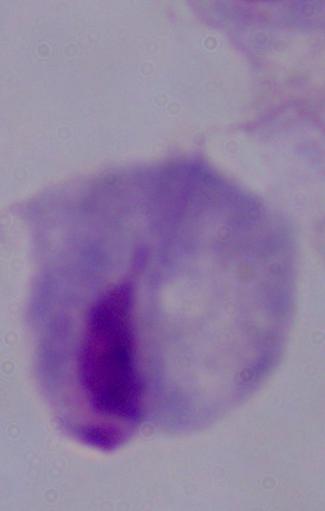
Micrograph. 1000x magnification. A trichomonad is seen.